Classify this cell by malaria status.
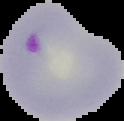
Parasitized.

Summary:
  - Preparation: thin blood film
  - Image type: segmented cell region with the area outside set to black
  - Image size: 124×121 pixels